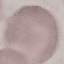

Malaria status: uninfected. Thin blood smear. Cell patch, automatically extracted from a larger field of view and resized to 64 × 64 pixels. Acquired by smartphone through the microscope eyepiece. Giemsa-stained preparation.